Report the malaria status of this cell.
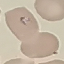
It is parasitized.

Summary:
  - Preparation: thin blood film
  - Capture: smartphone through the microscope eyepiece
  - Image type: cell patch, automatically extracted from a larger field of view and resized to 64 × 64 pixels
  - Stain: Giemsa